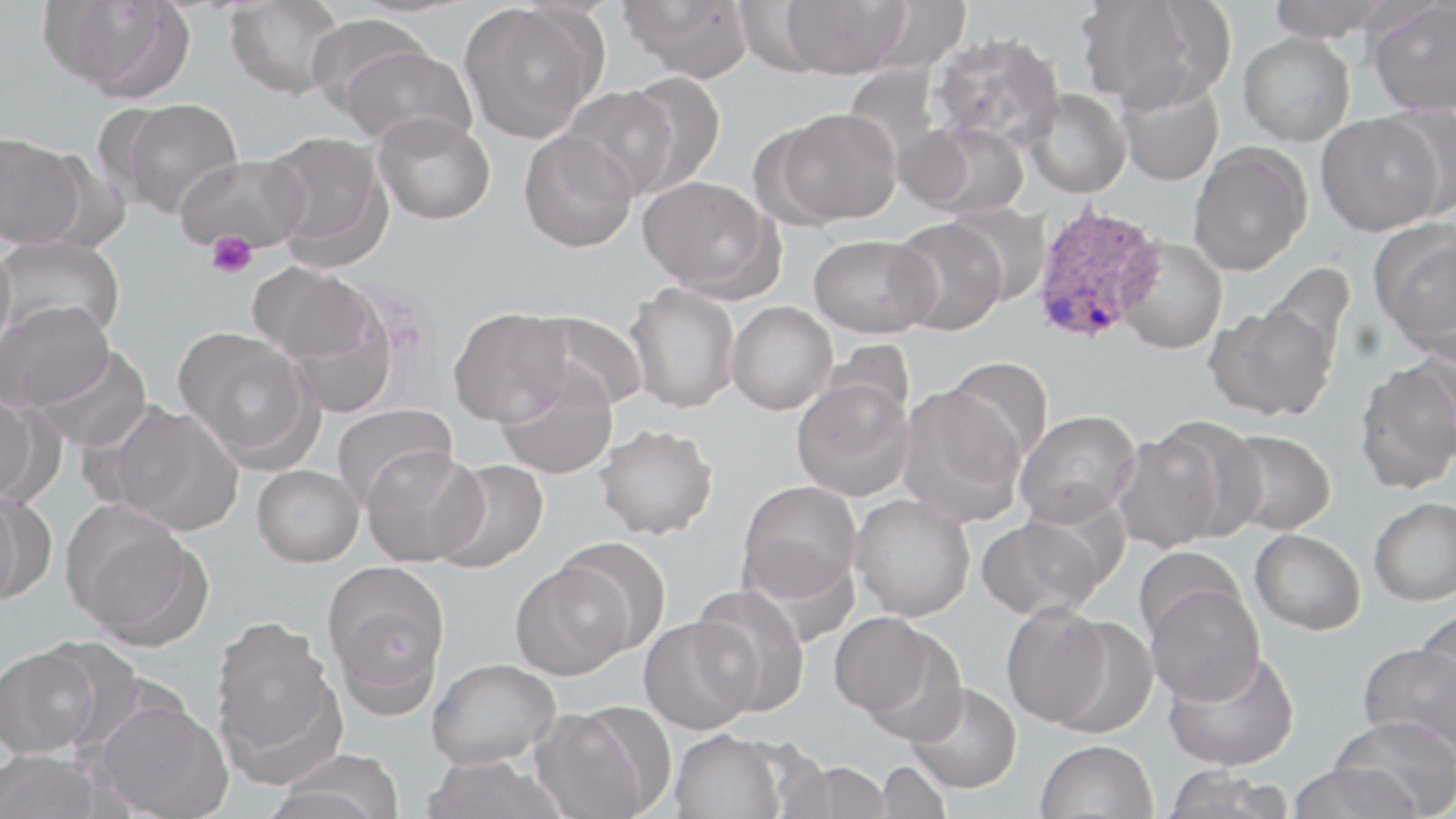 Approximate bounding boxes as named x1/y1/x2/y2 corners in pixels. Platelet locations: (x1=205, y1=231, x2=258, y2=279). Plasmodium ovale-infected red blood cell locations: (x1=1030, y1=202, x2=1163, y2=345). Uninfected red blood cell locations: (x1=38, y1=0, x2=187, y2=96), (x1=619, y1=0, x2=755, y2=81), (x1=780, y1=0, x2=909, y2=78), (x1=1265, y1=0, x2=1397, y2=42), (x1=1366, y1=0, x2=1456, y2=116), (x1=224, y1=1, x2=345, y2=99), (x1=864, y1=1, x2=972, y2=72), (x1=1076, y1=2, x2=1223, y2=111), (x1=459, y1=3, x2=603, y2=143), (x1=305, y1=14, x2=435, y2=119), (x1=929, y1=31, x2=1064, y2=151), (x1=1238, y1=32, x2=1355, y2=146), (x1=339, y1=45, x2=477, y2=151), (x1=617, y1=71, x2=725, y2=195), (x1=1115, y1=76, x2=1225, y2=187), (x1=561, y1=86, x2=678, y2=199), (x1=1023, y1=89, x2=1131, y2=198), (x1=115, y1=97, x2=244, y2=219), (x1=1375, y1=103, x2=1455, y2=221), (x1=772, y1=107, x2=901, y2=225), (x1=373, y1=113, x2=496, y2=225), (x1=1316, y1=113, x2=1440, y2=236), (x1=904, y1=121, x2=1029, y2=219), (x1=518, y1=130, x2=638, y2=253), (x1=263, y1=131, x2=393, y2=269), (x1=0, y1=132, x2=85, y2=249), (x1=1188, y1=143, x2=1312, y2=276), (x1=174, y1=154, x2=310, y2=255), (x1=638, y1=175, x2=780, y2=297), (x1=946, y1=203, x2=1052, y2=306), (x1=889, y1=217, x2=1008, y2=335), (x1=1370, y1=221, x2=1456, y2=357), (x1=809, y1=233, x2=936, y2=337), (x1=0, y1=236, x2=126, y2=343), (x1=1116, y1=237, x2=1227, y2=354), (x1=0, y1=242, x2=17, y2=365), (x1=1261, y1=262, x2=1356, y2=369), (x1=250, y1=264, x2=375, y2=365), (x1=625, y1=282, x2=741, y2=413), (x1=281, y1=286, x2=406, y2=418), (x1=3, y1=301, x2=114, y2=411), (x1=726, y1=301, x2=837, y2=415), (x1=1207, y1=301, x2=1338, y2=421), (x1=448, y1=307, x2=571, y2=427), (x1=524, y1=310, x2=650, y2=412), (x1=174, y1=327, x2=313, y2=460), (x1=820, y1=339, x2=915, y2=428), (x1=29, y1=344, x2=153, y2=452), (x1=1407, y1=344, x2=1456, y2=458), (x1=944, y1=356, x2=1054, y2=466), (x1=1354, y1=359, x2=1456, y2=492), (x1=494, y1=366, x2=618, y2=479), (x1=791, y1=379, x2=914, y2=501), (x1=897, y1=386, x2=1027, y2=526), (x1=0, y1=390, x2=39, y2=504), (x1=331, y1=402, x2=457, y2=509), (x1=112, y1=404, x2=245, y2=535), (x1=1015, y1=410, x2=1141, y2=527), (x1=1149, y1=417, x2=1268, y2=541), (x1=595, y1=424, x2=719, y2=539), (x1=1221, y1=429, x2=1336, y2=535), (x1=1112, y1=430, x2=1224, y2=553), (x1=361, y1=447, x2=487, y2=566), (x1=434, y1=459, x2=549, y2=574), (x1=252, y1=465, x2=364, y2=567), (x1=737, y1=480, x2=862, y2=603), (x1=0, y1=486, x2=22, y2=610), (x1=851, y1=494, x2=975, y2=621), (x1=1369, y1=497, x2=1456, y2=607), (x1=65, y1=506, x2=206, y2=645), (x1=976, y1=515, x2=1104, y2=620), (x1=1250, y1=529, x2=1366, y2=634), (x1=556, y1=537, x2=672, y2=655), (x1=1134, y1=546, x2=1246, y2=644), (x1=324, y1=561, x2=451, y2=709), (x1=511, y1=562, x2=632, y2=679), (x1=691, y1=584, x2=810, y2=715), (x1=1146, y1=584, x2=1264, y2=704), (x1=1001, y1=603, x2=1114, y2=729), (x1=1414, y1=607, x2=1456, y2=718), (x1=828, y1=611, x2=946, y2=724), (x1=638, y1=616, x2=757, y2=735), (x1=1048, y1=616, x2=1158, y2=739), (x1=210, y1=618, x2=342, y2=773), (x1=1358, y1=643, x2=1456, y2=760), (x1=1, y1=644, x2=102, y2=757), (x1=1163, y1=648, x2=1300, y2=771), (x1=427, y1=657, x2=560, y2=768), (x1=906, y1=682, x2=1022, y2=793), (x1=94, y1=698, x2=231, y2=819), (x1=531, y1=705, x2=663, y2=819), (x1=1330, y1=716, x2=1456, y2=817), (x1=669, y1=729, x2=788, y2=819), (x1=1036, y1=739, x2=1158, y2=819), (x1=0, y1=749, x2=108, y2=819), (x1=267, y1=751, x2=405, y2=819), (x1=421, y1=755, x2=564, y2=819), (x1=778, y1=759, x2=893, y2=819), (x1=876, y1=761, x2=950, y2=819), (x1=1286, y1=762, x2=1420, y2=819), (x1=1162, y1=765, x2=1294, y2=819). Slide-level diagnosis: Plasmodium ovale. Image is 1456×819 pixels. May-Grünwald-Giemsa stain. Thin blood film. Single field of view. Captured at 1000x magnification. Optical microscopy.